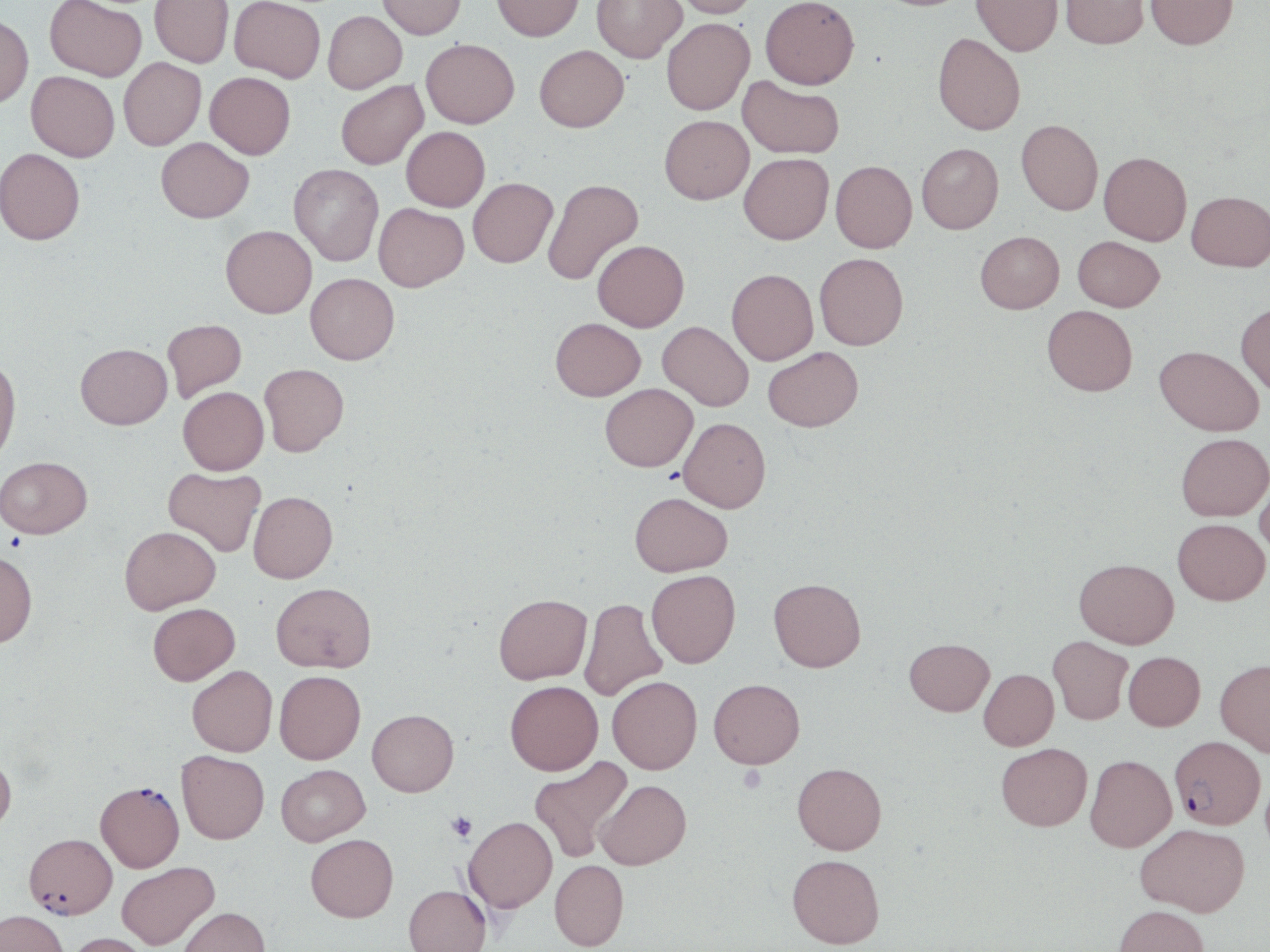
slide-level diagnosis = Plasmodium falciparum
uninfected red blood cell locations = approximate bounding boxes as (x1,y1)-(x2,y2) corner pairs in pixels: (45,0)-(147,81), (229,0)-(325,82), (377,0)-(466,39), (492,0)-(584,41), (592,0)-(687,62), (670,0)-(759,18), (760,0)-(860,89), (972,0)-(1063,56), (1059,0)-(1149,49), (1145,0)-(1239,49), (150,1)-(234,67), (323,11)-(407,93), (0,14)-(34,108), (661,18)-(754,115), (933,33)-(1026,135), (421,38)-(519,128), (535,45)-(628,132), (119,58)-(206,150), (26,71)-(120,161), (205,72)-(295,159), (738,75)-(844,159), (336,79)-(428,170), (659,115)-(753,204), (1016,119)-(1103,215), (401,126)-(490,212), (156,137)-(254,222), (917,143)-(1003,234), (0,148)-(85,244), (1099,151)-(1192,245), (739,153)-(834,244), (831,160)-(917,252), (289,164)-(384,266), (468,177)-(557,268), (542,178)-(644,287), (1187,190)-(1270,271), (374,203)-(469,292), (221,225)-(316,318), (975,231)-(1064,313), (1073,236)-(1165,311), (593,240)-(689,331), (814,253)-(908,350), (727,268)-(818,365), (306,273)-(399,364), (1236,302)-(1270,395), (1042,305)-(1137,396), (551,317)-(646,400), (163,319)-(246,402), (658,321)-(753,411), (75,343)-(172,429), (1155,345)-(1263,436), (763,346)-(863,431), (0,355)-(21,468), (260,363)-(349,456), (600,383)-(697,471), (178,386)-(269,475), (678,417)-(771,512), (1176,433)-(1270,521), (0,456)-(93,538), (163,467)-(266,556), (1255,469)-(1270,556), (249,491)-(337,583), (629,491)-(733,576), (1173,518)-(1269,605), (119,525)-(220,614), (0,549)-(38,647), (1074,558)-(1179,648), (647,570)-(741,667), (768,577)-(866,672), (271,582)-(376,672), (493,593)-(592,684), (580,597)-(667,701), (148,603)-(240,685), (1048,636)-(1133,724), (904,638)-(994,715), (1124,651)-(1205,731), (1215,658)-(1270,757), (187,665)-(278,756), (978,668)-(1058,750), (274,670)-(366,763), (608,676)-(702,774), (709,678)-(805,768), (505,680)-(603,775), (367,709)-(459,796), (996,743)-(1092,830), (176,750)-(269,844), (0,752)-(16,835), (1085,754)-(1177,851), (529,756)-(633,862), (792,762)-(886,854), (276,764)-(370,845), (595,779)-(691,869), (464,816)-(557,913), (1136,823)-(1250,916), (305,833)-(398,922), (787,854)-(885,948), (549,860)-(629,950), (116,861)-(219,949), (404,885)-(492,952), (1113,904)-(1209,952), (178,906)-(270,952), (0,909)-(68,952), (63,932)-(152,952)
modality = optical microscopy
stain = May-Grünwald-Giemsa
platelet locations = approximate bounding boxes as (x1,y1)-(x2,y2) corner pairs in pixels: (737,765)-(767,793), (447,811)-(478,842)
image size = 1270×952 pixels
Plasmodium falciparum-infected red blood cell locations = approximate bounding boxes as (x1,y1)-(x2,y2) corner pairs in pixels: (1170,735)-(1265,829), (95,780)-(184,872), (24,832)-(117,918)
magnification = 1000x
field of view = single
preparation = thin blood smear